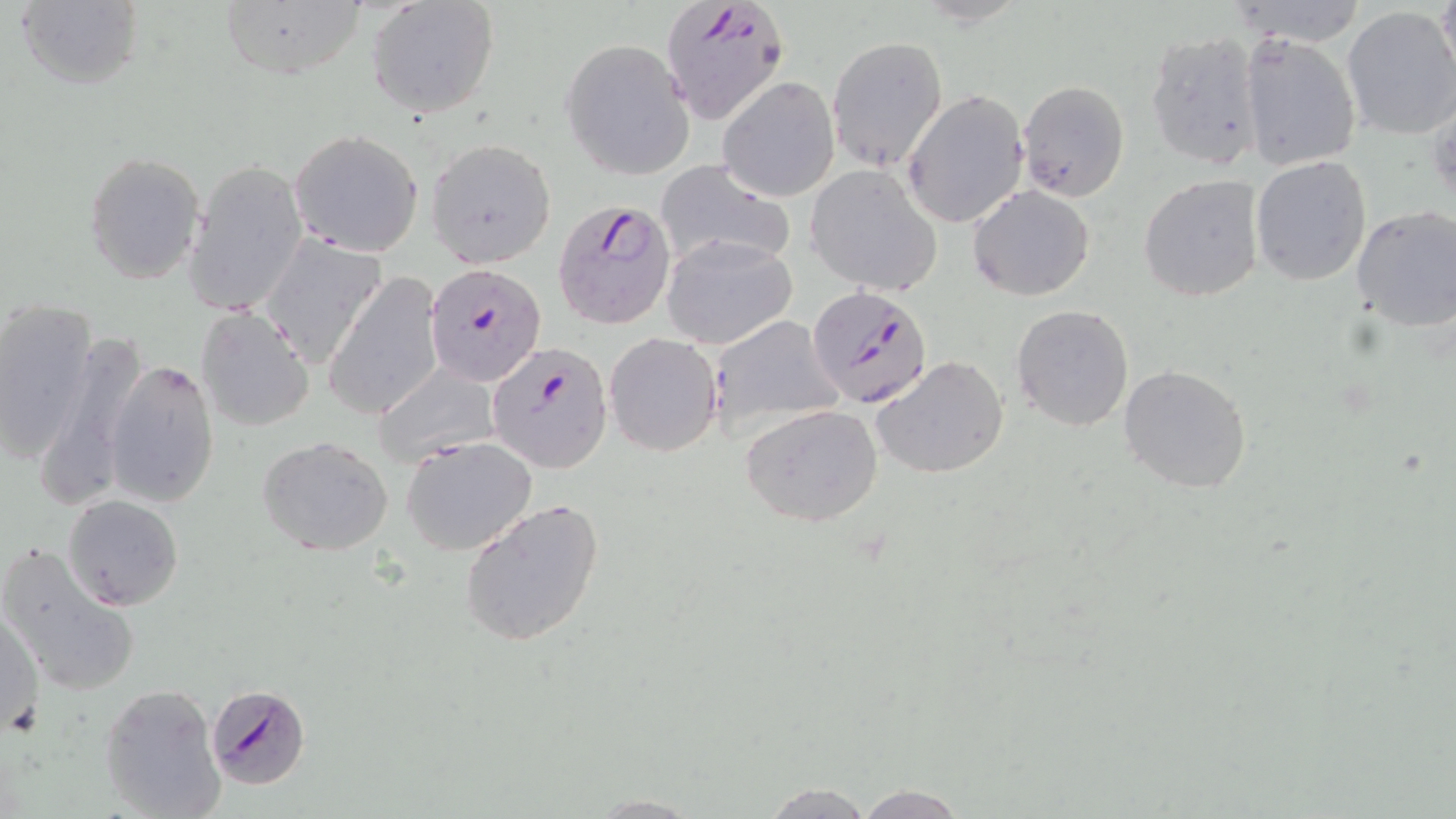
slide_level_diagnosis: Plasmodium falciparum
magnification: 1000x
uninfected_red_blood_cell_locations: 'approximate bounding boxes as named x1/y1/x2/y2 corners in pixels: (x1=366, y1=0, x2=500, y2=118), (x1=1432, y1=0, x2=1455, y2=88), (x1=13, y1=1, x2=145, y2=91), (x1=217, y1=2, x2=367, y2=81), (x1=1341, y1=6, x2=1456, y2=141), (x1=1141, y1=30, x2=1265, y2=171), (x1=1238, y1=34, x2=1361, y2=172), (x1=827, y1=35, x2=948, y2=172), (x1=560, y1=39, x2=695, y2=179), (x1=720, y1=78, x2=840, y2=201), (x1=1018, y1=80, x2=1130, y2=201), (x1=904, y1=90, x2=1029, y2=228), (x1=289, y1=128, x2=424, y2=257), (x1=427, y1=137, x2=557, y2=269), (x1=84, y1=150, x2=205, y2=286), (x1=1250, y1=155, x2=1372, y2=287), (x1=654, y1=158, x2=796, y2=274), (x1=185, y1=160, x2=307, y2=320), (x1=806, y1=165, x2=942, y2=295), (x1=1138, y1=174, x2=1264, y2=303), (x1=967, y1=185, x2=1095, y2=300), (x1=1352, y1=207, x2=1456, y2=333), (x1=258, y1=234, x2=387, y2=368), (x1=660, y1=234, x2=798, y2=350), (x1=325, y1=272, x2=446, y2=421), (x1=0, y1=299, x2=97, y2=463), (x1=1011, y1=303, x2=1136, y2=432), (x1=195, y1=306, x2=315, y2=432), (x1=707, y1=315, x2=843, y2=439), (x1=39, y1=328, x2=154, y2=507), (x1=603, y1=332, x2=722, y2=457), (x1=872, y1=355, x2=1009, y2=480), (x1=105, y1=359, x2=220, y2=507), (x1=371, y1=363, x2=503, y2=470), (x1=1118, y1=364, x2=1253, y2=494), (x1=740, y1=404, x2=883, y2=529), (x1=257, y1=435, x2=394, y2=557), (x1=401, y1=436, x2=537, y2=556), (x1=63, y1=494, x2=184, y2=609), (x1=459, y1=497, x2=606, y2=648), (x1=1, y1=541, x2=142, y2=699), (x1=2, y1=608, x2=44, y2=733), (x1=100, y1=684, x2=227, y2=819), (x1=757, y1=781, x2=877, y2=819), (x1=851, y1=783, x2=972, y2=819), (x1=588, y1=793, x2=704, y2=816)'
preparation: thin blood film
stain: May-Grünwald-Giemsa
plasmodium_falciparum_infected_red_blood_cell_locations: 'approximate bounding boxes as named x1/y1/x2/y2 corners in pixels: (x1=659, y1=0, x2=791, y2=126), (x1=552, y1=197, x2=678, y2=329), (x1=426, y1=262, x2=546, y2=387), (x1=807, y1=284, x2=934, y2=409), (x1=489, y1=341, x2=611, y2=471), (x1=209, y1=685, x2=311, y2=790)'
field_of_view: one of a larger specimen
modality: light microscopy
image_size: 1456×819 pixels